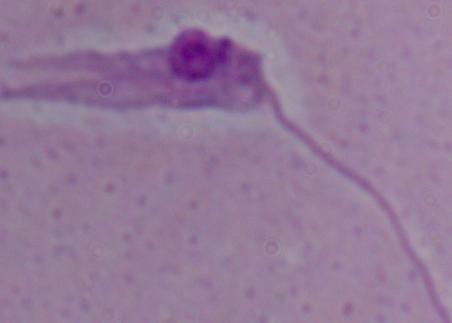
identification: Leishmania
magnification: 1000x
modality: photomicrograph